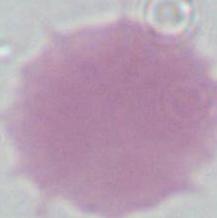

modality = photomicrograph
identification = erythrocyte
magnification = 1000x